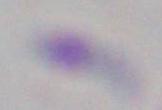

{
  "magnification": "1000x",
  "modality": "photomicrograph",
  "identification": "Toxoplasma gondii"
}